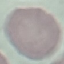
Result: negative for malaria parasites. Automatically extracted cell patch, resized to 64 × 64 pixels. Photographed with a smartphone camera at the microscope eyepiece. Giemsa-stained preparation. Thin blood smear.